Locate every Plasmodium falciparum-infected red blood cell.
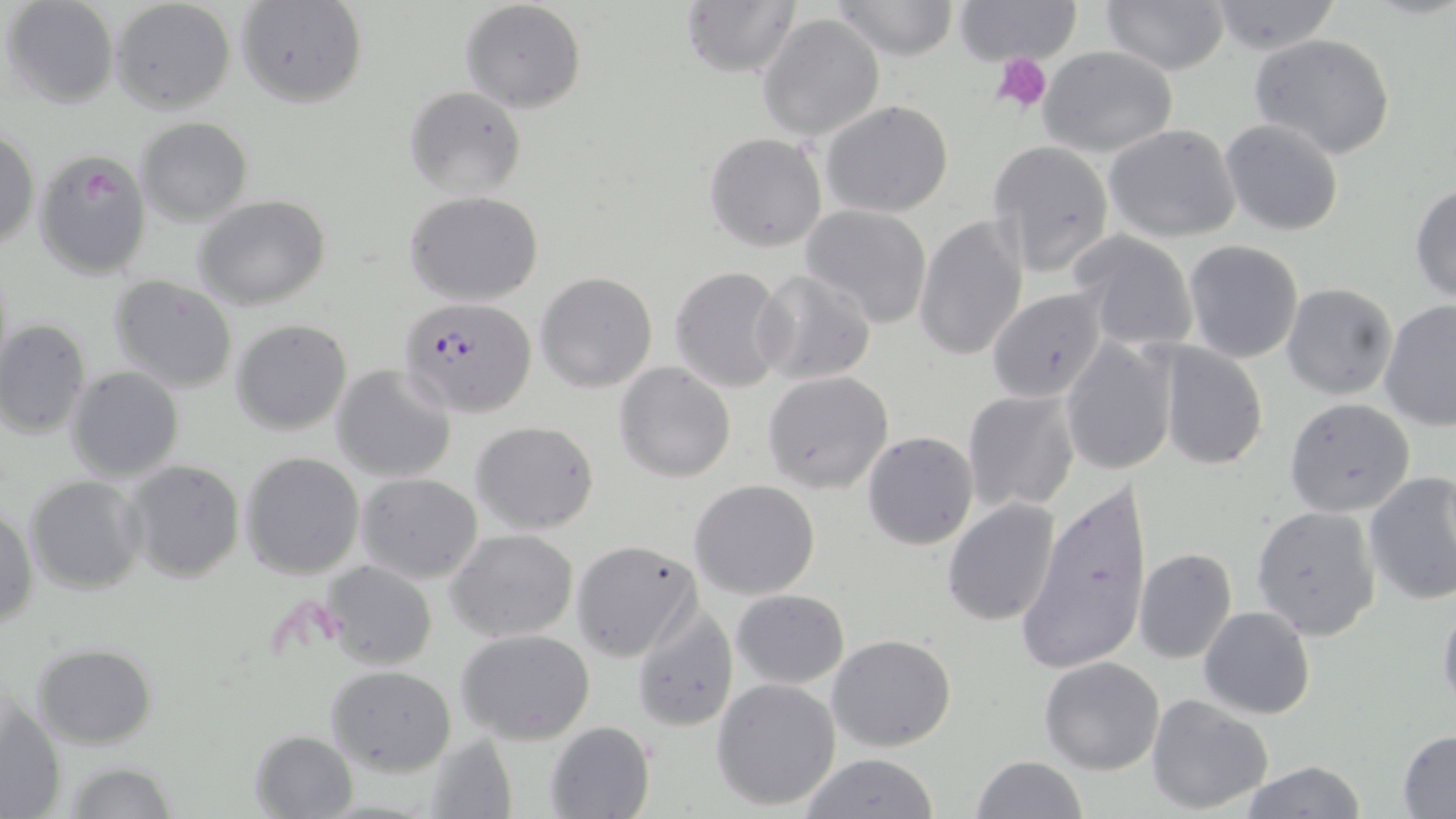
Approximate bounding boxes as [x1, y1, x2, y2] in pixels.
Plasmodium falciparum-infected red blood cells: [399, 296, 536, 417].

slide-level diagnosis = Plasmodium falciparum
modality = light microscopy
field of view = one of a larger specimen
stain = May-Grünwald-Giemsa
platelet locations = approximate bounding boxes as [x1, y1, x2, y2] in pixels: [991, 53, 1052, 112]
magnification = 1000x
image size = 1456×819 pixels
preparation = thin blood smear
uninfected red blood cell locations = approximate bounding boxes as [x1, y1, x2, y2] in pixels: [3, 0, 120, 108], [109, 0, 235, 113], [831, 0, 960, 59], [950, 0, 1085, 64], [1100, 0, 1232, 73], [233, 1, 368, 109], [460, 1, 587, 115], [682, 1, 798, 79], [1202, 2, 1343, 54], [758, 13, 885, 141], [1249, 33, 1396, 158], [1039, 47, 1178, 157], [403, 85, 526, 199], [820, 99, 954, 219], [135, 118, 253, 224], [1219, 118, 1346, 237], [1103, 124, 1243, 243], [1, 128, 40, 249], [704, 133, 828, 253], [985, 138, 1116, 278], [32, 147, 154, 280], [1409, 182, 1456, 305], [403, 189, 544, 306], [193, 195, 332, 310], [798, 204, 934, 327], [915, 215, 1029, 364], [1067, 229, 1199, 353], [1183, 239, 1305, 364], [0, 259, 14, 386], [669, 265, 788, 393], [752, 269, 875, 386], [534, 272, 657, 392], [108, 274, 238, 393], [1282, 284, 1399, 401], [985, 288, 1112, 404], [1379, 301, 1456, 431], [0, 319, 91, 441], [231, 319, 353, 436], [1059, 336, 1179, 476], [1155, 342, 1268, 469], [614, 361, 738, 482], [332, 365, 456, 482], [65, 366, 185, 482], [762, 370, 895, 493], [960, 390, 1082, 517], [1284, 397, 1416, 517], [470, 420, 600, 535], [861, 430, 979, 550], [240, 451, 365, 578], [123, 459, 245, 583], [357, 472, 484, 584], [1363, 472, 1456, 610], [23, 475, 147, 593], [688, 479, 822, 600], [1019, 479, 1152, 672], [942, 498, 1063, 626], [1250, 505, 1383, 640], [1, 506, 37, 631], [446, 528, 580, 644], [571, 539, 702, 661], [1134, 547, 1237, 665], [322, 560, 439, 670], [730, 589, 849, 688], [1437, 597, 1456, 717], [629, 601, 739, 733], [1198, 605, 1316, 720], [456, 629, 597, 745], [828, 635, 957, 753], [31, 643, 159, 749], [1039, 655, 1165, 774], [326, 665, 457, 776], [711, 678, 840, 811], [1146, 694, 1274, 812], [1, 698, 66, 819], [543, 721, 656, 819], [250, 729, 359, 818], [1397, 729, 1456, 816], [418, 736, 515, 819], [797, 752, 941, 819], [971, 755, 1089, 819], [60, 761, 178, 818], [1240, 761, 1369, 818]